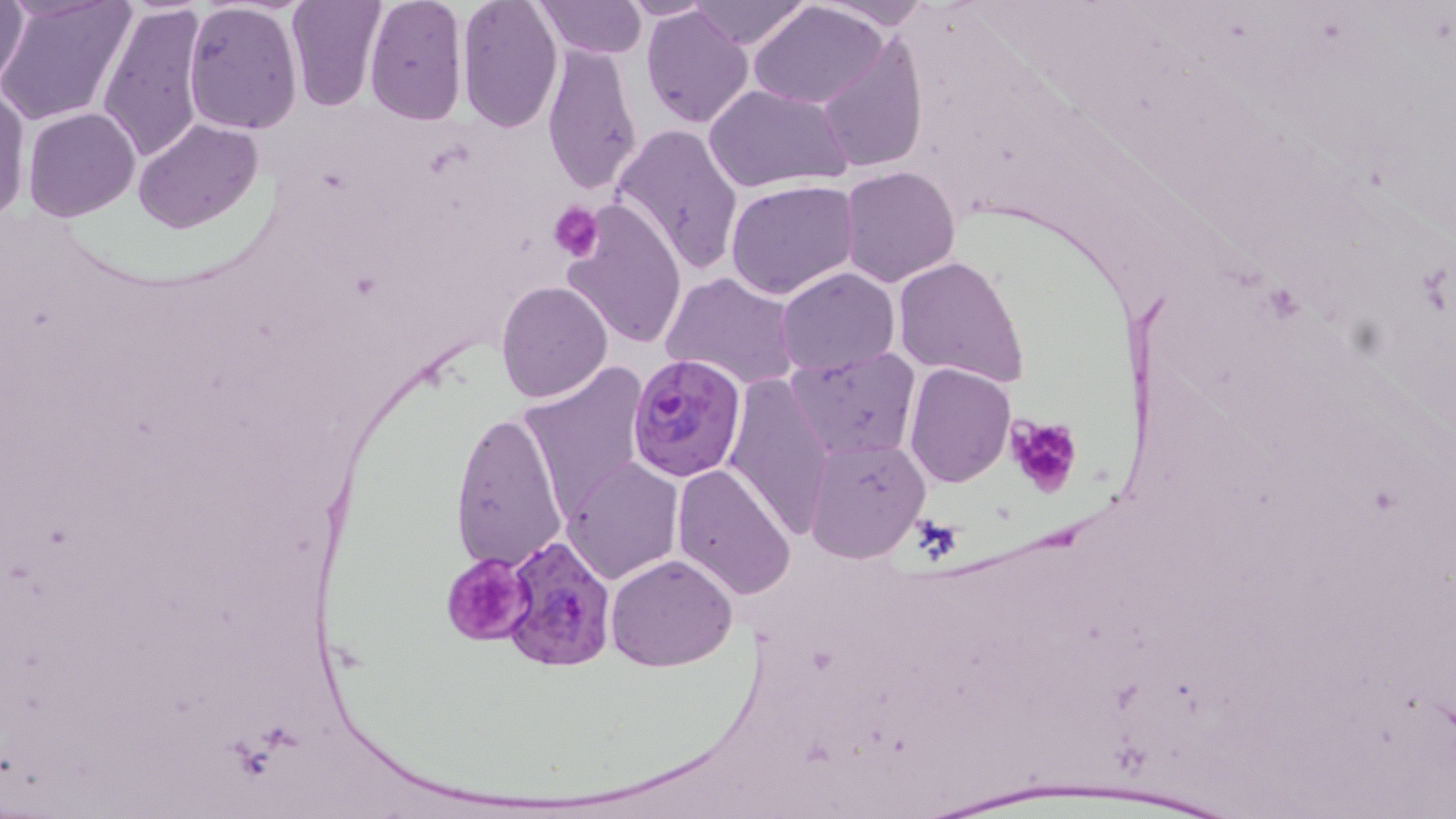

slide-level diagnosis = Plasmodium falciparum
platelet locations = approximate bounding boxes as (x1, y1, x2, y2) in pixels: (547, 201, 605, 264), (1005, 415, 1081, 498), (441, 552, 536, 647)
Plasmodium falciparum-infected red blood cell locations = approximate bounding boxes as (x1, y1, x2, y2) in pixels: (625, 353, 746, 481), (503, 536, 616, 669)
stain = May-Grünwald-Giemsa
modality = optical microscopy
magnification = 1000x
uninfected red blood cell locations = approximate bounding boxes as (x1, y1, x2, y2) in pixels: (0, 0, 31, 95), (0, 0, 134, 127), (285, 0, 387, 111), (454, 0, 563, 134), (535, 0, 646, 58), (617, 0, 720, 20), (687, 0, 812, 47), (812, 0, 934, 32), (362, 1, 469, 125), (96, 2, 210, 165), (183, 2, 303, 135), (751, 4, 887, 109), (639, 7, 753, 129), (810, 33, 929, 173), (541, 40, 642, 198), (0, 81, 30, 225), (705, 84, 851, 193), (22, 107, 140, 221), (133, 119, 262, 233), (609, 122, 745, 276), (839, 165, 961, 287), (726, 178, 859, 299), (559, 200, 689, 349), (892, 255, 1031, 388), (775, 267, 900, 379), (660, 272, 803, 391), (496, 281, 613, 403), (784, 347, 922, 462), (904, 362, 1015, 486), (517, 363, 652, 522), (723, 372, 834, 543), (447, 408, 569, 575), (803, 434, 930, 562), (560, 458, 685, 585), (672, 464, 798, 600), (606, 554, 736, 672)
field of view = single
preparation = thin blood smear
image size = 1456×819 pixels